Report the malaria status of this cell.
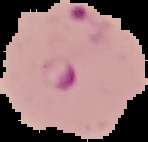

Parasitized.

image_type: segmented cell region on a black background
image_size: 148×142 pixels
preparation: thin blood smear